Assess this cell for malaria.
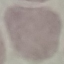

Uninfected.

Photographed with a smartphone camera at the microscope eyepiece. Thin blood smear. Giemsa-stained preparation. Automatically extracted cell patch, resized to 64 × 64 pixels.